Comment on the background quality.
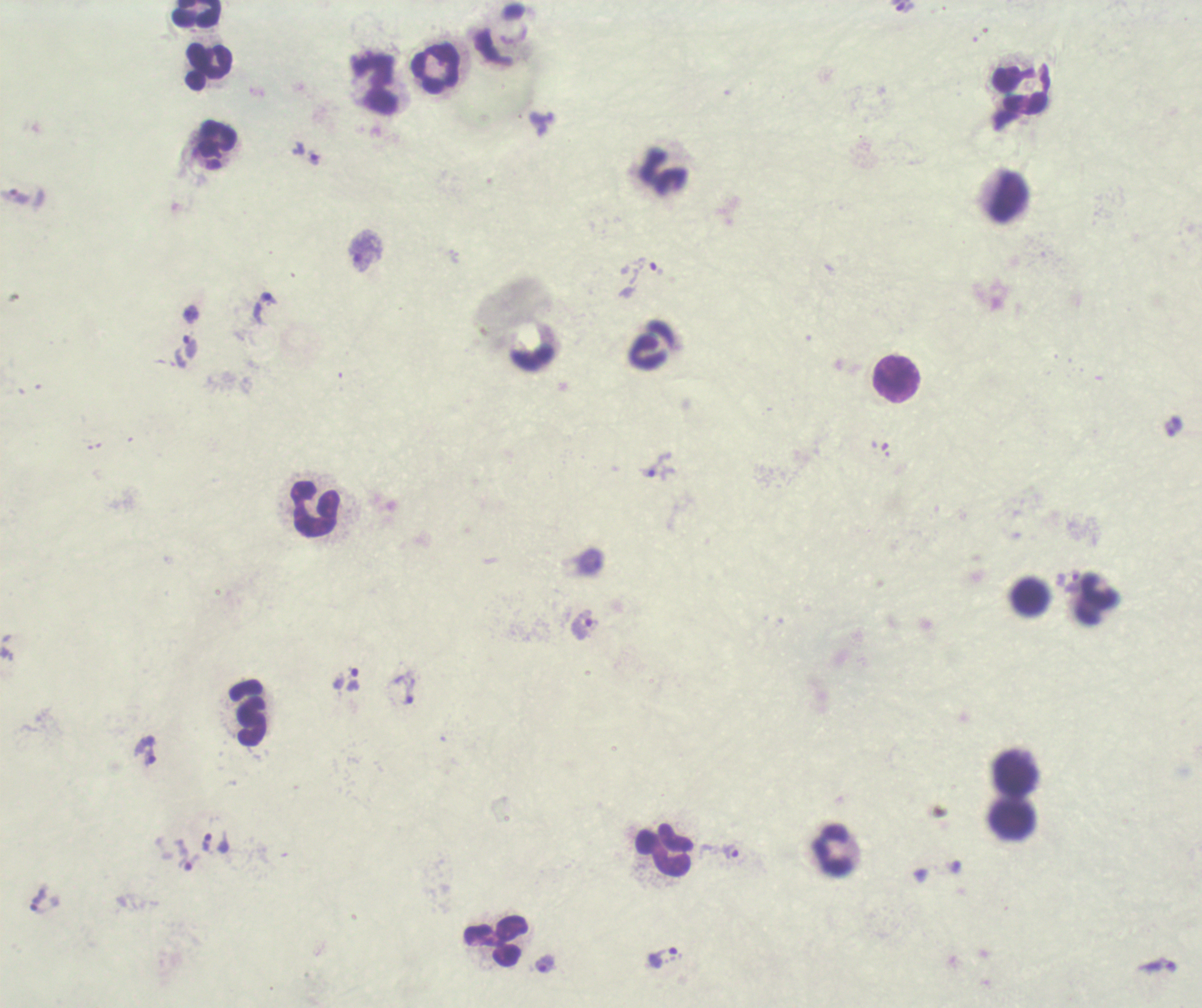
Unsatisfactory.

Approximate centers as [x, y] in pixels.
Summary:
  - Leukocyte locations: [198, 14], [210, 67], [435, 68], [375, 83], [1020, 89], [217, 139], [663, 171], [1006, 196], [650, 345], [897, 380], [316, 509], [1029, 597], [1096, 601], [247, 713], [1017, 773], [1013, 819], [664, 851], [832, 852], [495, 942]
  - Trophozoite locations: [314, 158], [190, 314], [189, 347], [657, 465], [584, 624], [353, 681], [406, 689], [143, 751], [206, 842], [731, 851], [184, 855], [37, 900], [662, 957], [545, 965]
  - Magnification: 100x
  - Preparation: thick smear of blood
  - Field of view: single
  - Result: malaria parasites detected
  - Context: previously used in a real diagnosis
  - Coloration quality: bad
  - Stain: Romanowsky
  - Image size: 1202×1008 pixels